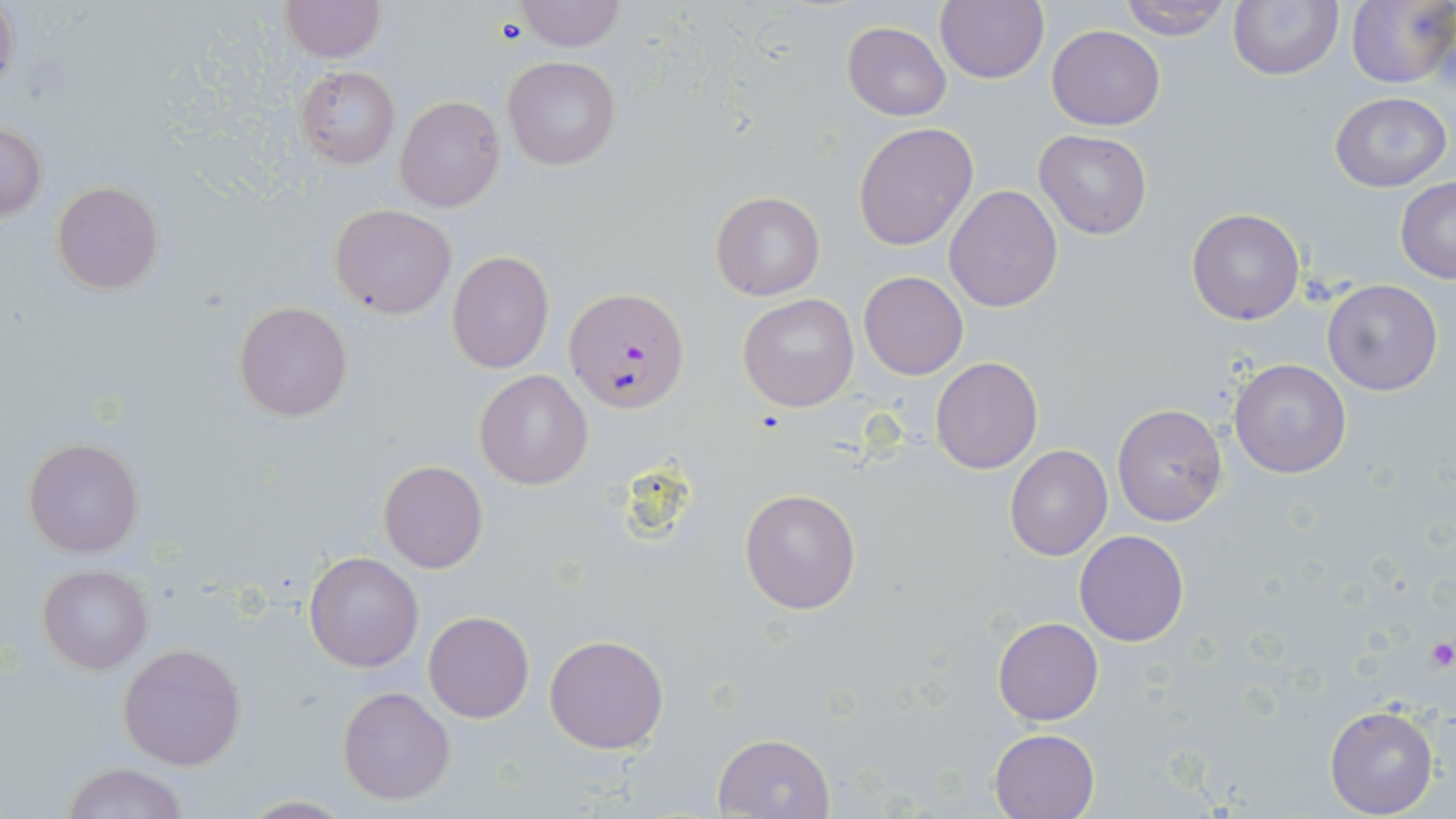
slide_level_diagnosis: Plasmodium falciparum
platelet_locations: 'approximate bounding boxes as (x1,y1)-(x2,y2) corner pairs in pixels: (1423,636)-(1455,671)'
modality: light microscopy
magnification: 1000x
field_of_view: one of a larger specimen
plasmodium_falciparum_infected_red_blood_cell_locations: 'approximate bounding boxes as (x1,y1)-(x2,y2) corner pairs in pixels: (566,287)-(691,412)'
image_size: 1456×819 pixels
stain: May-Grünwald-Giemsa
preparation: thin blood film
uninfected_red_blood_cell_locations: 'approximate bounding boxes as (x1,y1)-(x2,y2) corner pairs in pixels: (0,0)-(18,96), (280,0)-(384,62), (512,0)-(624,51), (935,0)-(1050,86), (1115,0)-(1233,40), (1228,0)-(1342,81), (1346,1)-(1455,88), (842,21)-(951,120), (1047,25)-(1165,129), (503,56)-(621,169), (295,66)-(400,168), (1330,92)-(1450,192), (394,95)-(504,211), (0,122)-(47,220), (853,122)-(978,250), (1034,130)-(1152,240), (1396,178)-(1456,282), (52,183)-(163,295), (944,185)-(1062,312), (710,191)-(824,301), (330,204)-(456,318), (1187,208)-(1305,326), (448,250)-(553,373), (858,270)-(969,380), (1320,280)-(1443,396), (737,293)-(858,412), (234,301)-(352,422), (930,356)-(1043,474), (1228,358)-(1352,478), (474,369)-(594,491), (1111,403)-(1228,526), (21,435)-(145,560), (1005,444)-(1112,560), (378,460)-(488,573), (738,487)-(861,615), (1074,529)-(1189,647), (304,552)-(423,672), (38,565)-(153,674), (424,611)-(534,724), (993,616)-(1104,725), (544,635)-(669,754), (118,643)-(247,770), (336,684)-(457,805), (1324,703)-(1439,817), (989,728)-(1098,819), (712,732)-(836,819), (61,762)-(190,819), (236,796)-(356,817)'